Evaluate for malaria.
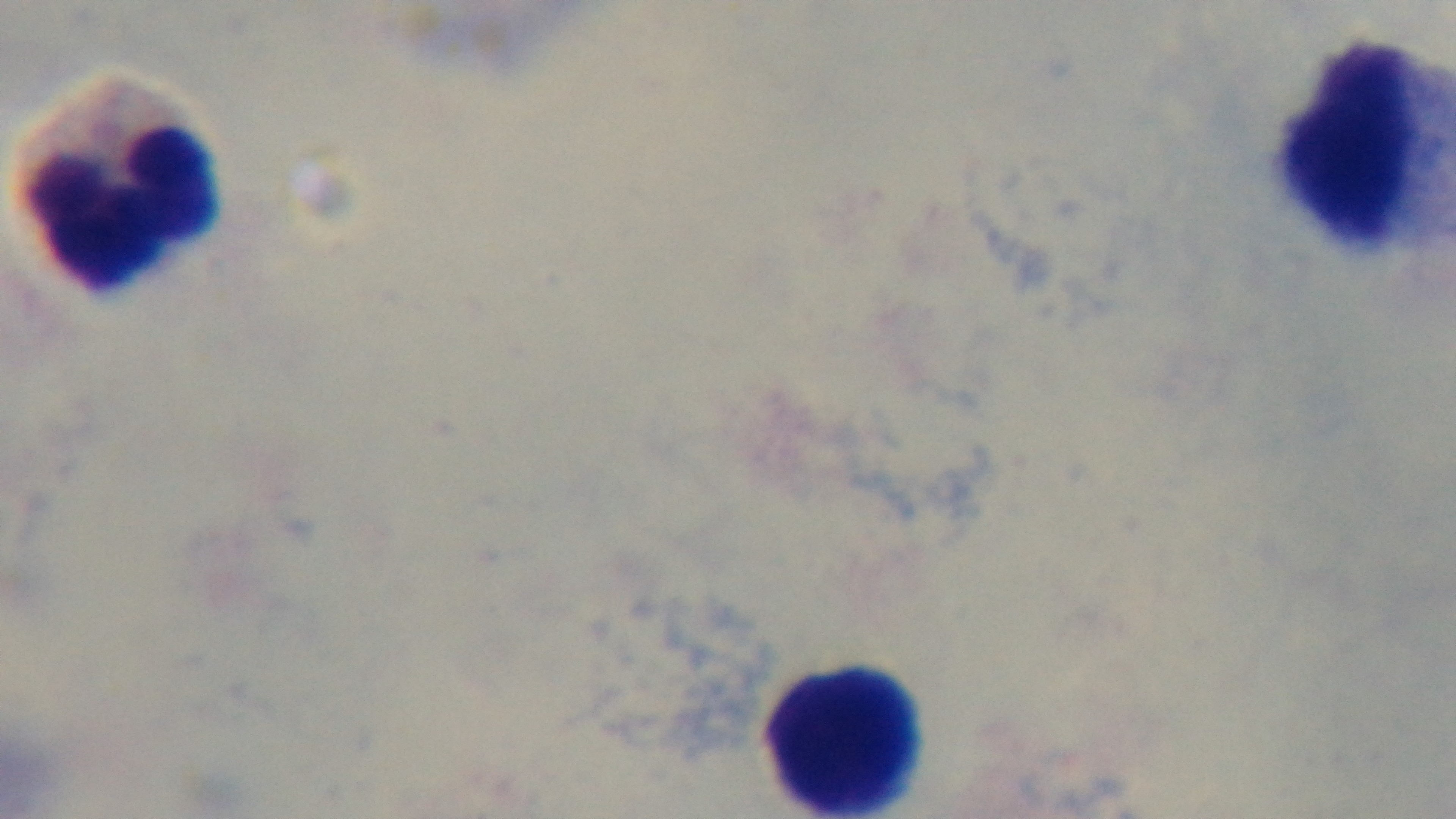

It is uninfected.

Giemsa-stained. Photomicrograph. Mounted 4K digital camera. Oil-immersion objective, 100x. Preparation: thick. One field from the slide.